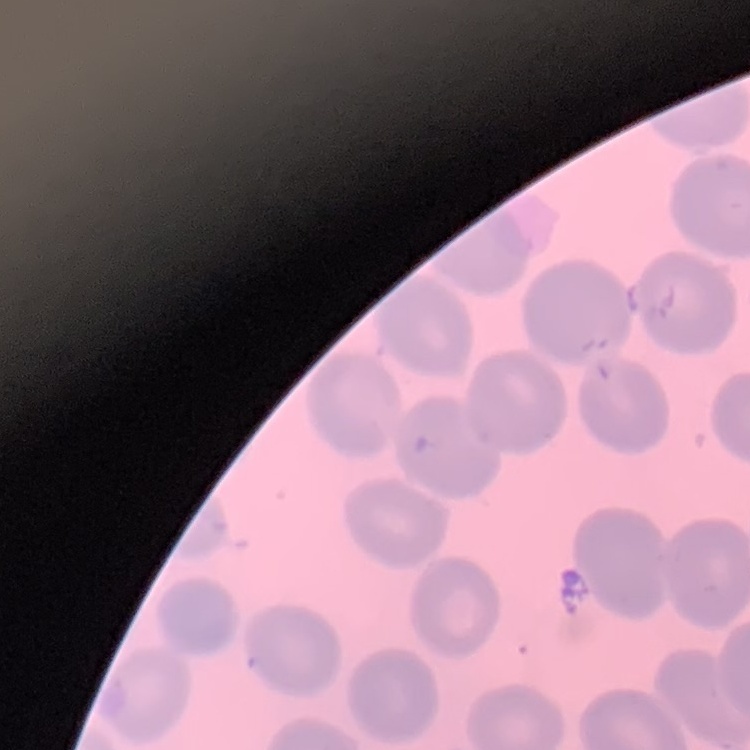 The red blood cells show no rouleaux formation. Thin blood film. Field's or Giemsa stain. Square crop of a larger photomicrograph.